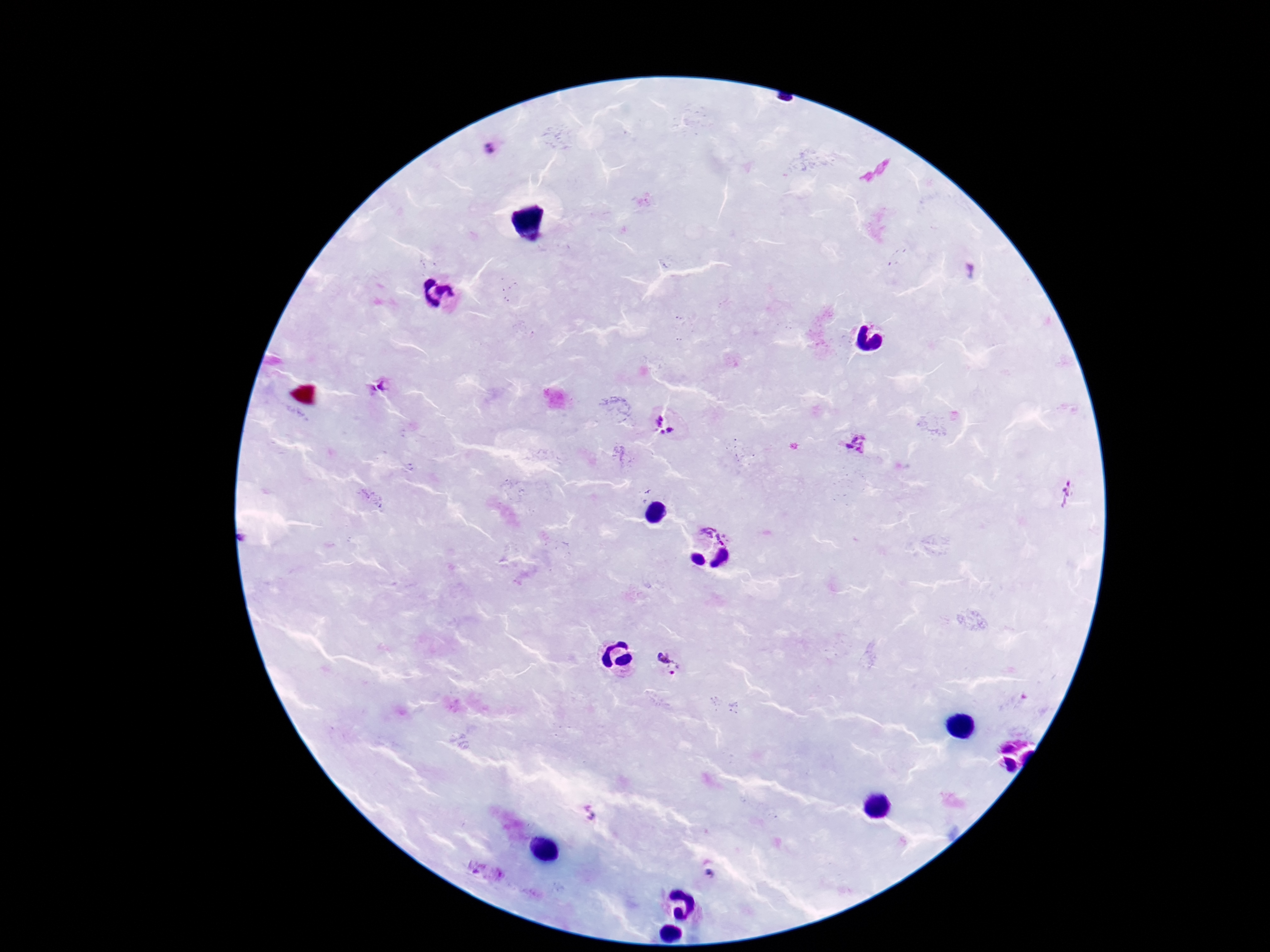

Approximate centers as [x, y] in pixels. Plasmodium parasite locations: [488, 149], [380, 388], [666, 423], [857, 444], [1067, 493], [718, 528], [670, 666], [590, 815], [487, 872]. Giemsa stain. Photographed through the microscope eyepiece with a smartphone camera. One field from this slide. Patient malaria status: infected. Thick peripheral-blood smear. Image is 1270×952 pixels. 100x magnification.